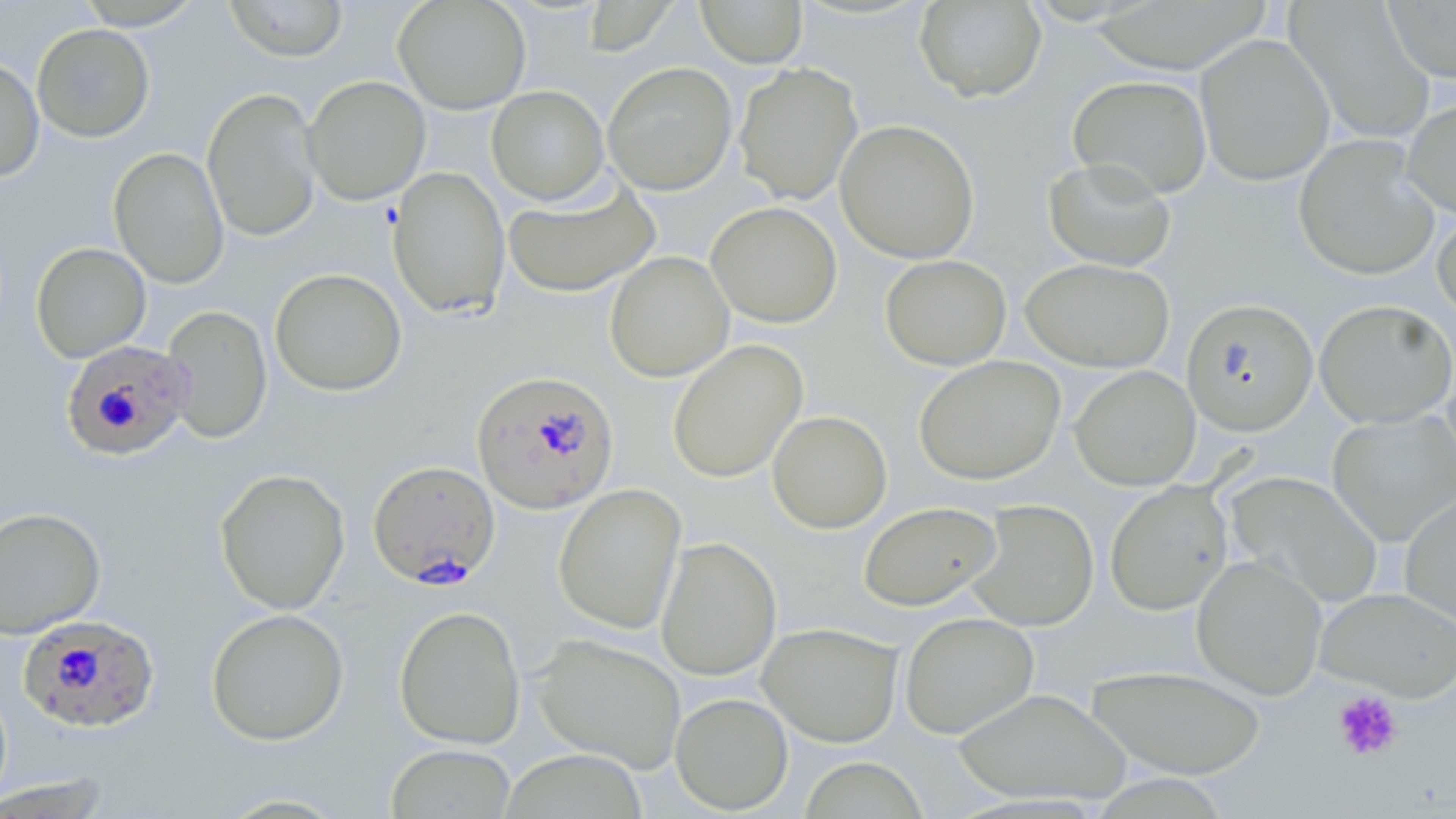
slide_level_diagnosis: Plasmodium falciparum
preparation: thin blood smear
field_of_view: single
uninfected_red_blood_cell_locations: 'approximate bounding boxes as named x1/y1/x2/y2 corners in pixels: (x1=224, y1=0, x2=349, y2=61), (x1=393, y1=0, x2=531, y2=114), (x1=1382, y1=0, x2=1456, y2=83), (x1=72, y1=1, x2=206, y2=30), (x1=580, y1=1, x2=676, y2=56), (x1=696, y1=1, x2=807, y2=68), (x1=913, y1=1, x2=1046, y2=103), (x1=1285, y1=2, x2=1435, y2=144), (x1=31, y1=23, x2=155, y2=142), (x1=1195, y1=33, x2=1335, y2=186), (x1=0, y1=57, x2=44, y2=182), (x1=602, y1=61, x2=738, y2=195), (x1=734, y1=63, x2=863, y2=205), (x1=1068, y1=74, x2=1213, y2=199), (x1=303, y1=75, x2=430, y2=205), (x1=487, y1=85, x2=610, y2=205), (x1=202, y1=87, x2=323, y2=243), (x1=1402, y1=96, x2=1456, y2=220), (x1=834, y1=119, x2=980, y2=264), (x1=1293, y1=135, x2=1440, y2=281), (x1=109, y1=146, x2=230, y2=288), (x1=1042, y1=157, x2=1177, y2=271), (x1=387, y1=166, x2=511, y2=320), (x1=503, y1=177, x2=661, y2=298), (x1=705, y1=201, x2=843, y2=328), (x1=1433, y1=207, x2=1456, y2=323), (x1=31, y1=242, x2=151, y2=363), (x1=604, y1=251, x2=734, y2=382), (x1=880, y1=254, x2=1011, y2=370), (x1=1020, y1=257, x2=1174, y2=372), (x1=269, y1=268, x2=407, y2=396), (x1=1181, y1=298, x2=1319, y2=436), (x1=1315, y1=299, x2=1455, y2=428), (x1=161, y1=305, x2=273, y2=443), (x1=667, y1=339, x2=808, y2=483), (x1=914, y1=355, x2=1066, y2=485), (x1=1070, y1=365, x2=1200, y2=490), (x1=767, y1=410, x2=892, y2=533), (x1=1327, y1=410, x2=1456, y2=546), (x1=214, y1=468, x2=350, y2=615), (x1=1226, y1=470, x2=1384, y2=610), (x1=1105, y1=481, x2=1232, y2=615), (x1=553, y1=484, x2=687, y2=634), (x1=1399, y1=492, x2=1456, y2=630), (x1=966, y1=498, x2=1099, y2=631), (x1=858, y1=501, x2=1002, y2=611), (x1=0, y1=506, x2=106, y2=639), (x1=656, y1=536, x2=782, y2=680), (x1=1191, y1=554, x2=1328, y2=699), (x1=1314, y1=586, x2=1456, y2=701), (x1=394, y1=605, x2=526, y2=749), (x1=205, y1=607, x2=349, y2=746), (x1=899, y1=612, x2=1039, y2=738), (x1=757, y1=622, x2=903, y2=746), (x1=531, y1=634, x2=687, y2=773), (x1=1086, y1=665, x2=1267, y2=779), (x1=951, y1=687, x2=1134, y2=805), (x1=670, y1=692, x2=793, y2=814), (x1=386, y1=744, x2=518, y2=818), (x1=798, y1=756, x2=930, y2=819)'
magnification: 1000x
image_size: 1456×819 pixels
platelet_locations: 'approximate bounding boxes as named x1/y1/x2/y2 corners in pixels: (x1=1331, y1=689, x2=1403, y2=762)'
plasmodium_falciparum_infected_red_blood_cell_locations: 'approximate bounding boxes as named x1/y1/x2/y2 corners in pixels: (x1=60, y1=337, x2=192, y2=464), (x1=471, y1=370, x2=619, y2=514), (x1=367, y1=459, x2=501, y2=589), (x1=18, y1=614, x2=161, y2=734)'
stain: May-Grünwald-Giemsa
modality: light microscopy